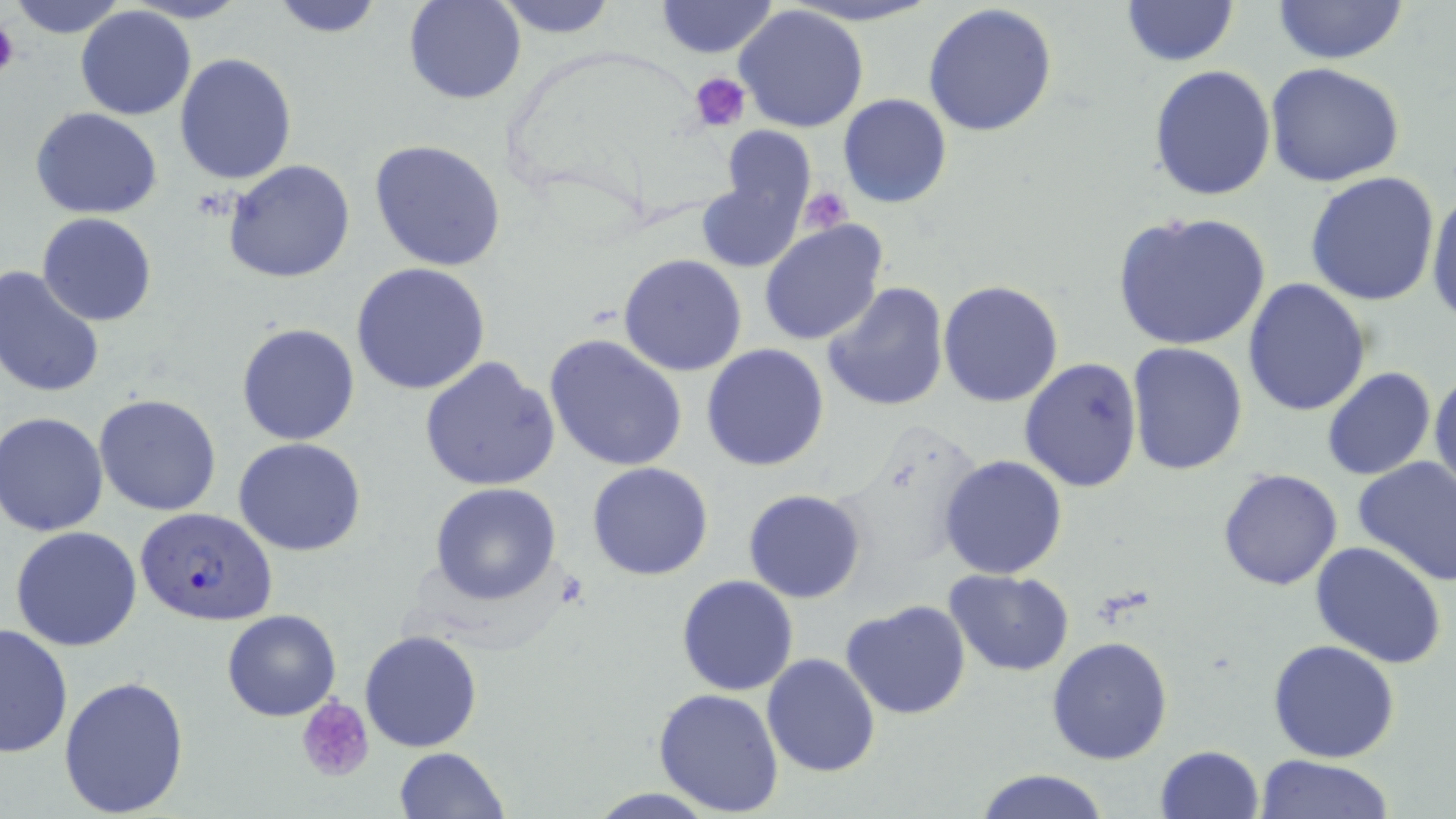

slide-level diagnosis = Plasmodium falciparum
stain = May-Grünwald-Giemsa
magnification = 1000x
uninfected red blood cell locations = approximate bounding boxes as named x1/y1/x2/y2 corners in pixels: (x1=6, y1=0, x2=133, y2=40), (x1=267, y1=0, x2=388, y2=38), (x1=404, y1=0, x2=526, y2=104), (x1=492, y1=0, x2=620, y2=38), (x1=655, y1=0, x2=779, y2=57), (x1=1119, y1=1, x2=1239, y2=67), (x1=1269, y1=1, x2=1411, y2=66), (x1=923, y1=3, x2=1059, y2=137), (x1=736, y1=5, x2=870, y2=133), (x1=75, y1=6, x2=196, y2=122), (x1=174, y1=53, x2=297, y2=185), (x1=1264, y1=62, x2=1408, y2=187), (x1=1149, y1=64, x2=1276, y2=200), (x1=837, y1=95, x2=952, y2=209), (x1=30, y1=107, x2=164, y2=218), (x1=719, y1=127, x2=816, y2=230), (x1=368, y1=139, x2=510, y2=272), (x1=223, y1=159, x2=355, y2=283), (x1=696, y1=166, x2=809, y2=276), (x1=1304, y1=171, x2=1441, y2=306), (x1=1425, y1=185, x2=1456, y2=329), (x1=1111, y1=211, x2=1271, y2=352), (x1=36, y1=212, x2=157, y2=326), (x1=759, y1=221, x2=889, y2=349), (x1=619, y1=253, x2=748, y2=376), (x1=351, y1=262, x2=493, y2=397), (x1=0, y1=267, x2=105, y2=399), (x1=1241, y1=277, x2=1371, y2=416), (x1=938, y1=279, x2=1066, y2=407), (x1=823, y1=281, x2=950, y2=412), (x1=236, y1=322, x2=361, y2=446), (x1=546, y1=333, x2=690, y2=472), (x1=1125, y1=342, x2=1249, y2=476), (x1=700, y1=343, x2=829, y2=471), (x1=419, y1=357, x2=560, y2=491), (x1=1019, y1=357, x2=1143, y2=493), (x1=1429, y1=366, x2=1456, y2=502), (x1=1322, y1=367, x2=1436, y2=480), (x1=93, y1=393, x2=222, y2=516), (x1=2, y1=412, x2=111, y2=537), (x1=233, y1=438, x2=367, y2=555), (x1=939, y1=455, x2=1068, y2=579), (x1=1352, y1=456, x2=1456, y2=586), (x1=587, y1=462, x2=713, y2=582), (x1=1217, y1=468, x2=1344, y2=591), (x1=430, y1=482, x2=563, y2=605), (x1=743, y1=490, x2=867, y2=604), (x1=9, y1=525, x2=143, y2=651), (x1=1308, y1=542, x2=1447, y2=671), (x1=945, y1=569, x2=1074, y2=675), (x1=676, y1=574, x2=799, y2=695), (x1=840, y1=599, x2=970, y2=720), (x1=222, y1=609, x2=342, y2=722), (x1=774, y1=616, x2=958, y2=758), (x1=0, y1=621, x2=75, y2=759), (x1=360, y1=629, x2=485, y2=752), (x1=1047, y1=636, x2=1172, y2=765), (x1=1267, y1=639, x2=1400, y2=762), (x1=761, y1=652, x2=881, y2=779), (x1=59, y1=675, x2=189, y2=815), (x1=652, y1=687, x2=785, y2=814), (x1=1154, y1=745, x2=1265, y2=819), (x1=394, y1=746, x2=509, y2=819), (x1=1258, y1=755, x2=1392, y2=818), (x1=972, y1=769, x2=1112, y2=819)
Plasmodium falciparum-infected red blood cell locations = approximate bounding boxes as named x1/y1/x2/y2 corners in pixels: (x1=134, y1=506, x2=278, y2=628)
image size = 1456×819 pixels
field of view = single
modality = optical microscopy
platelet locations = approximate bounding boxes as named x1/y1/x2/y2 corners in pixels: (x1=663, y1=2, x2=772, y2=57), (x1=0, y1=16, x2=19, y2=81), (x1=690, y1=72, x2=751, y2=131), (x1=798, y1=189, x2=851, y2=236), (x1=295, y1=694, x2=377, y2=785)
preparation = thin blood film